Locate every blood parasite and identify its species.
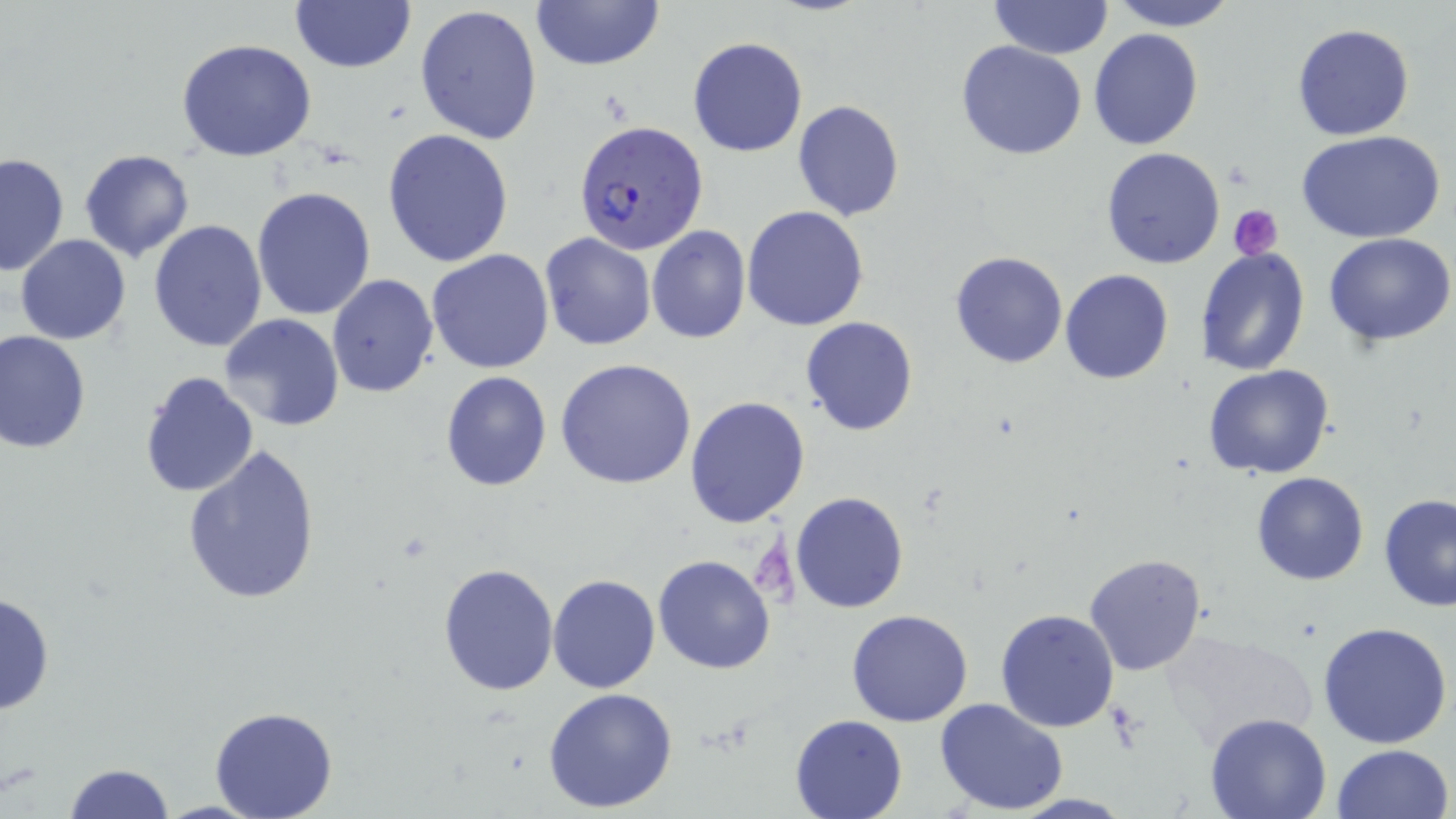

Approximate bounding boxes as [x1, y1, x2, y2] in pixels.
Plasmodium falciparum-infected red blood cells: [574, 120, 709, 257].
No Plasmodium ovale, Plasmodium malariae, Plasmodium vivax, Babesia divergens, or Trypanosoma brucei observed.

Platelet locations: [1228, 204, 1284, 261]. Uninfected red blood cell locations: [988, 0, 1112, 59], [1104, 0, 1242, 31], [530, 1, 665, 73], [290, 2, 416, 74], [414, 4, 545, 146], [1292, 22, 1414, 140], [1088, 28, 1205, 149], [688, 35, 809, 158], [174, 37, 317, 162], [955, 40, 1088, 160], [791, 100, 906, 221], [382, 129, 514, 268], [1298, 130, 1447, 242], [1101, 147, 1225, 269], [78, 148, 195, 262], [0, 153, 69, 277], [252, 186, 378, 322], [742, 205, 870, 331], [148, 220, 269, 353], [646, 227, 750, 344], [1324, 232, 1454, 348], [15, 234, 130, 344], [540, 234, 655, 350], [1195, 246, 1310, 377], [427, 249, 555, 374], [949, 250, 1068, 368], [1060, 268, 1173, 384], [326, 274, 439, 397], [217, 314, 345, 432], [800, 316, 919, 436], [1, 330, 91, 455], [555, 358, 698, 488], [1204, 365, 1335, 480], [138, 370, 260, 499], [439, 371, 552, 492], [684, 397, 811, 528], [182, 443, 321, 606], [1251, 472, 1368, 586], [790, 491, 909, 612], [1378, 494, 1456, 612], [652, 554, 776, 675], [1084, 554, 1209, 677], [438, 562, 560, 697], [548, 573, 661, 693], [0, 591, 54, 716], [994, 607, 1121, 732], [846, 608, 975, 727], [1318, 621, 1454, 749], [1161, 629, 1317, 751], [541, 686, 680, 812], [935, 697, 1069, 816], [210, 706, 337, 819], [791, 713, 907, 818], [1202, 713, 1332, 819], [1330, 742, 1454, 819], [64, 762, 176, 819]. Slide-level diagnosis: Plasmodium falciparum. May-Grünwald-Giemsa-stained preparation. One field of a larger specimen. Light microscopy. Image is 1456×819 pixels. Thin blood film. Captured at 1000x magnification.